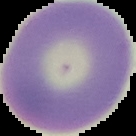
The area outside the segmented cell region is set to black. Result: no malaria parasites seen. From a thin blood smear. Image is 136×136 pixels.